Locate and identify every blood parasite.
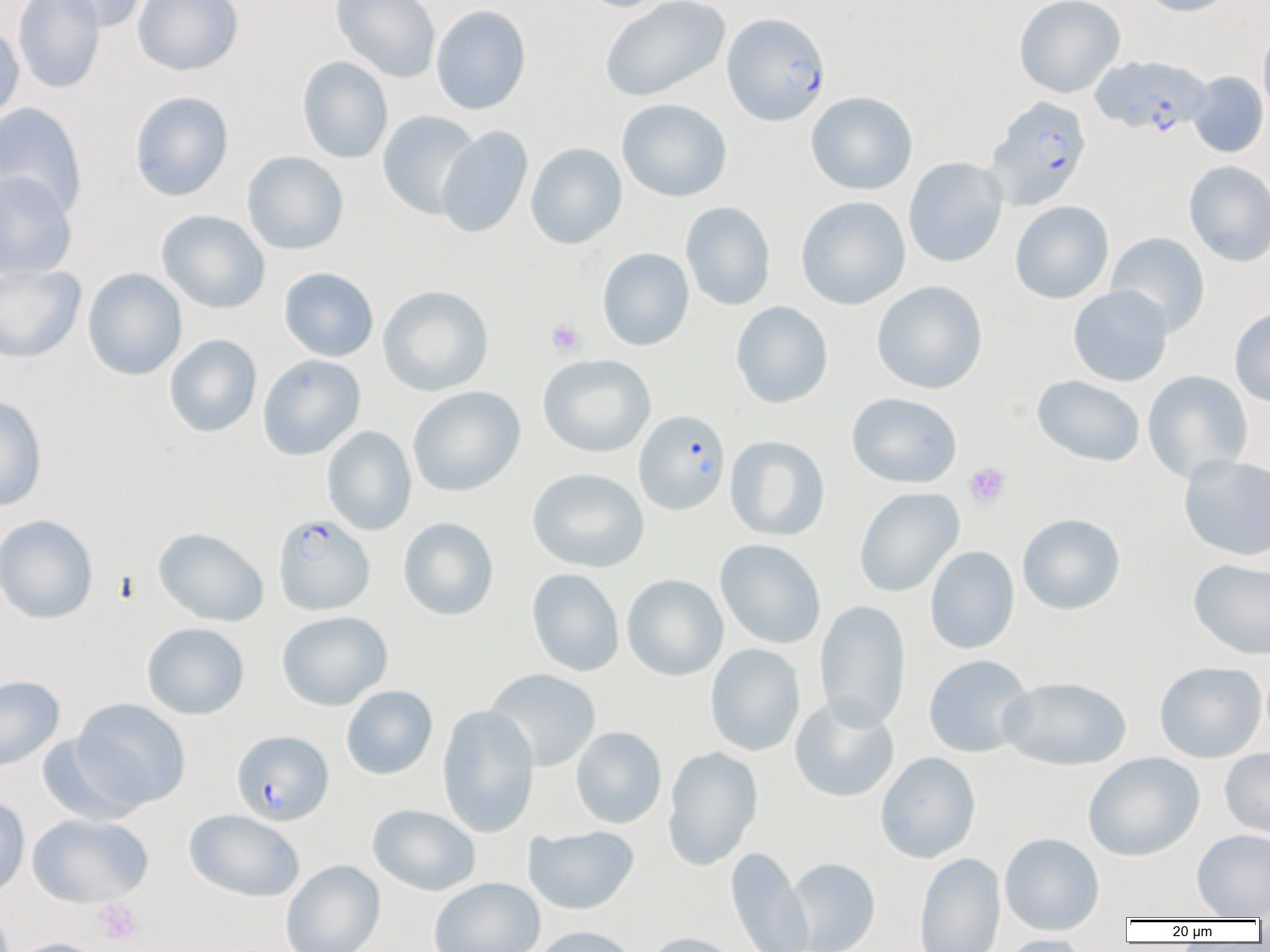

Approximate bounding boxes as (x1,y1)-(x2,y2) corner pairs in pixels.
Plasmodium falciparum-infected red blood cells: (722,12)-(830,125), (1092,55)-(1211,137), (985,96)-(1092,210), (634,409)-(730,516), (273,513)-(374,615), (231,730)-(333,826).
No Plasmodium ovale, Plasmodium malariae, Plasmodium vivax, Babesia divergens, or Trypanosoma brucei observed.

slide-level diagnosis = Plasmodium falciparum
uninfected red blood cell locations = approximate bounding boxes as (x1,y1)-(x2,y2) corner pairs in pixels: (12,0)-(105,94), (50,0)-(148,33), (132,0)-(244,76), (329,0)-(441,82), (577,0)-(676,13), (599,0)-(731,102), (1014,0)-(1125,98), (1138,0)-(1238,17), (431,4)-(531,115), (0,21)-(25,125), (1257,23)-(1270,125), (296,55)-(393,164), (1187,71)-(1269,158), (129,91)-(234,201), (805,91)-(918,195), (616,98)-(732,202), (0,102)-(87,218), (377,110)-(481,219), (435,126)-(533,238), (525,142)-(627,249), (242,150)-(349,254), (904,157)-(1008,268), (1184,160)-(1270,266), (0,170)-(77,280), (796,195)-(911,310), (680,201)-(776,311), (1010,201)-(1113,304), (156,210)-(270,314), (1106,232)-(1210,336), (597,248)-(694,351), (0,263)-(86,364), (82,267)-(187,381), (279,267)-(379,362), (871,280)-(988,394), (378,285)-(494,396), (1067,285)-(1174,387), (731,301)-(833,409), (1229,306)-(1270,407), (164,334)-(262,438), (257,354)-(366,460), (537,354)-(656,457), (1142,370)-(1253,483), (1032,374)-(1146,467), (408,386)-(525,497), (846,392)-(962,488), (0,395)-(48,512), (321,426)-(417,536), (725,435)-(830,541), (1178,454)-(1270,560), (527,468)-(649,573), (854,487)-(964,597), (1017,512)-(1125,615), (0,514)-(99,624), (398,517)-(498,621), (152,527)-(269,627), (715,539)-(826,649), (925,545)-(1020,654), (1188,558)-(1270,660), (526,568)-(625,677), (622,574)-(728,681), (815,600)-(911,730), (276,611)-(392,711), (141,622)-(250,720), (704,643)-(805,756), (923,654)-(1034,758), (1154,661)-(1266,763), (484,668)-(601,772), (0,675)-(65,772), (997,676)-(1131,771), (341,685)-(438,780), (789,696)-(900,802), (70,698)-(190,810), (437,705)-(539,838), (570,726)-(667,829), (37,733)-(144,824), (662,746)-(762,870), (1220,747)-(1270,840), (875,751)-(981,863), (1083,752)-(1205,861), (0,793)-(30,899), (368,804)-(481,896), (184,809)-(304,902), (27,813)-(154,908), (524,825)-(640,914), (1192,829)-(1270,918), (999,832)-(1104,936), (726,846)-(813,951), (914,852)-(1005,952), (785,858)-(880,952), (281,859)-(385,952), (429,877)-(545,952), (531,925)-(641,952), (640,932)-(745,952), (1000,935)-(1093,952), (7,938)-(109,952)
image size = 1270×952 pixels
modality = optical microscopy
preparation = thin blood smear
platelet locations = approximate bounding boxes as (x1,y1)-(x2,y2) corner pairs in pixels: (546,320)-(584,355), (963,462)-(1011,509), (94,898)-(143,945)
field of view = single
magnification = 1000x